Locate every leukocyte (white blood cell).
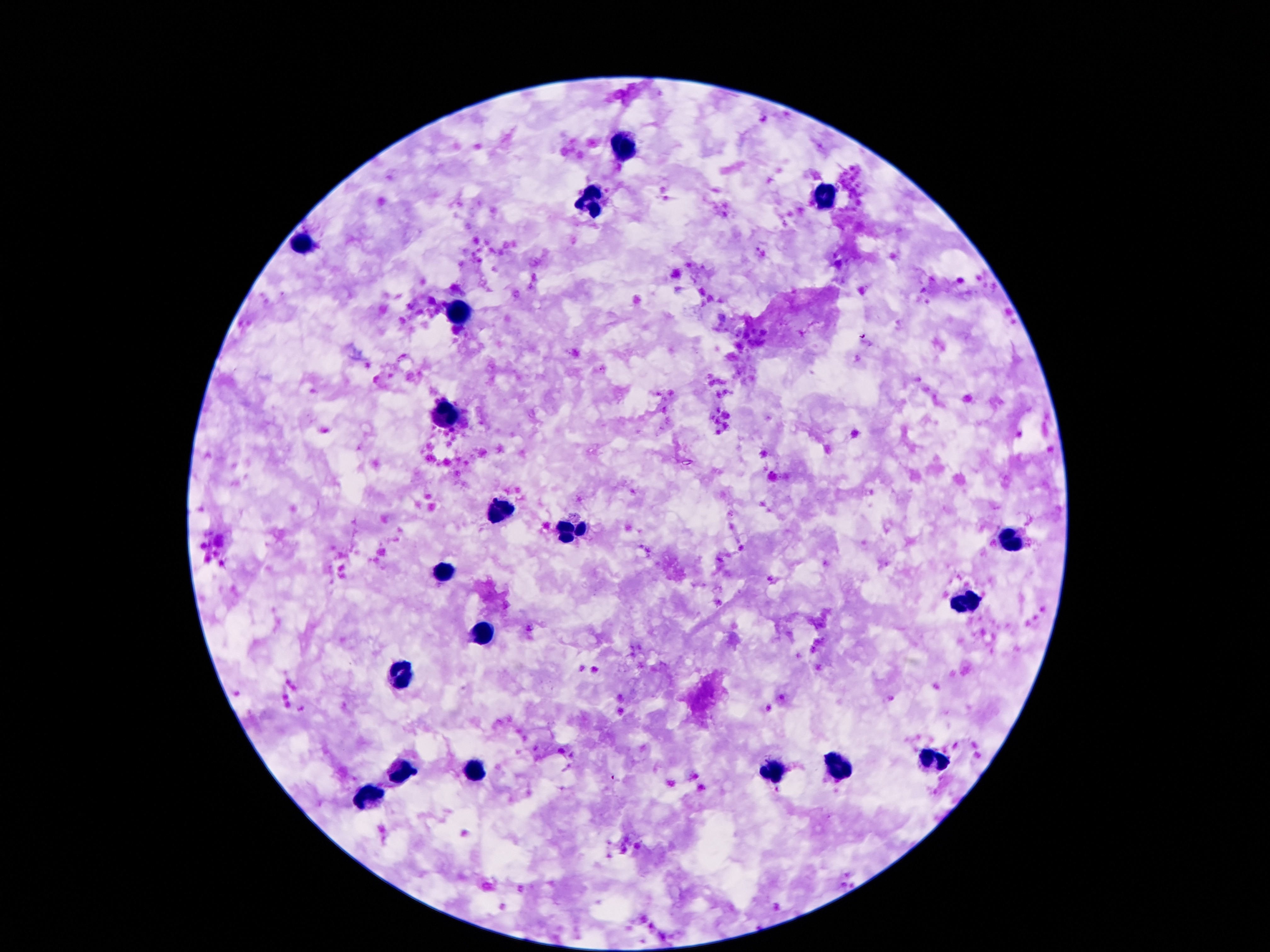
Approximate object centers, in pixels from the top-left corner.
Leukocytes: (x=620, y=148), (x=824, y=195), (x=589, y=202), (x=301, y=243), (x=463, y=310), (x=448, y=413), (x=496, y=510), (x=570, y=536), (x=1009, y=540), (x=442, y=571), (x=964, y=600), (x=484, y=635), (x=402, y=677), (x=931, y=762), (x=473, y=767), (x=839, y=767), (x=773, y=770), (x=398, y=772), (x=370, y=798).

Summary:
  - Preparation: thick blood smear
  - Stain: Giemsa
  - Capture: smartphone camera through the microscope eyepiece
  - Image size: 1270×952 pixels
  - Magnification: 100x
  - Patient malaria status: negative
  - Field of view: single